Classify the preparation.
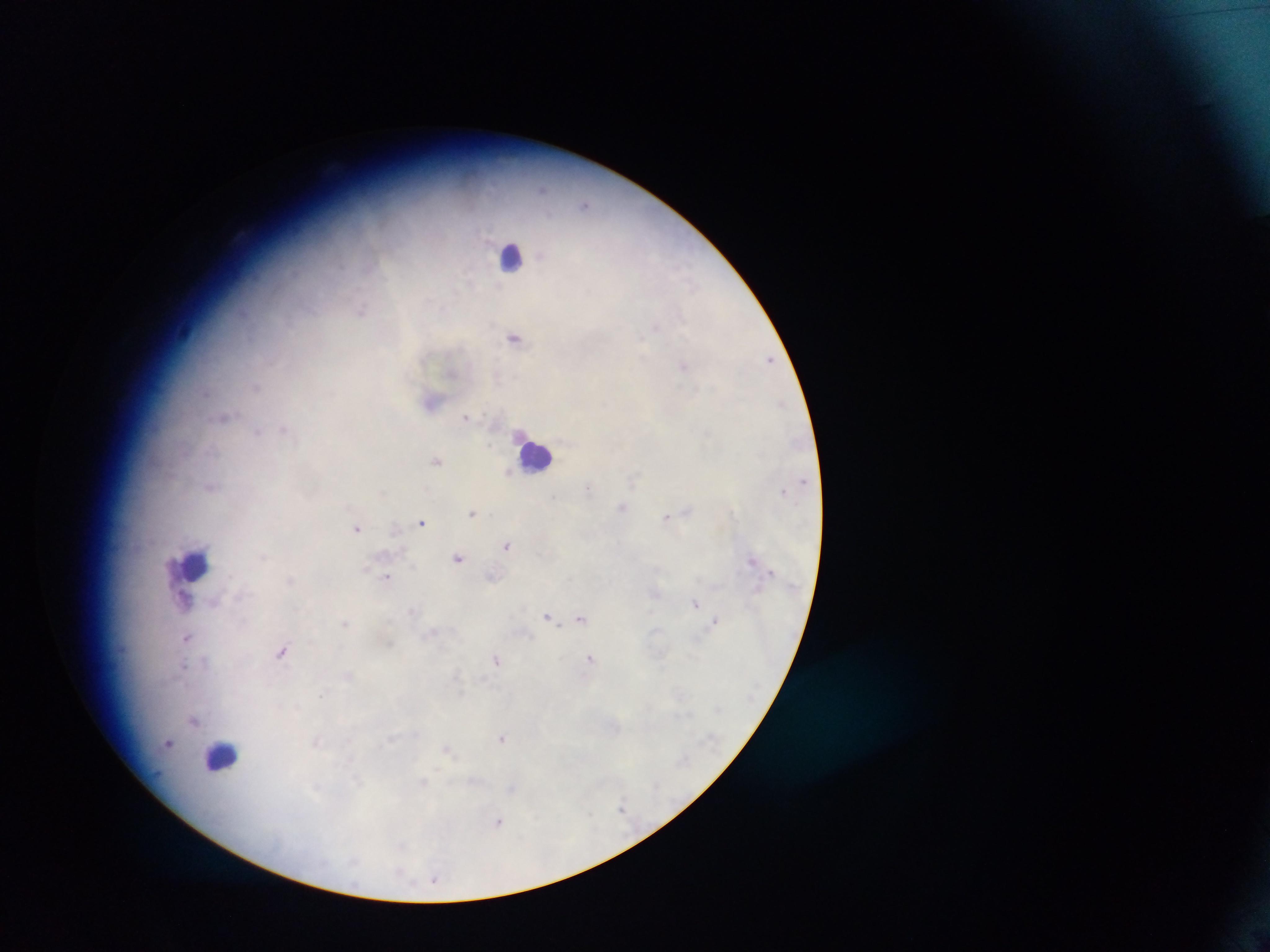
This is a thick smear.

Approximate centers as x y in pixels.
Summary:
  - Plasmodium parasite locations: 545 188; 584 204; 362 307; 680 314; 655 326; 515 337; 772 360; 686 366; 257 385; 695 389; 223 416; 466 417; 283 427; 257 431; 710 436; 438 461; 509 472; 209 485; 590 489; 555 496; 622 507; 688 510; 733 511; 470 513; 666 516; 422 521; 356 528; 506 545; 264 558; 457 559; 752 560; 387 576; 290 579; 187 596; 214 602; 695 602; 547 614; 582 616; 716 620; 345 623; 186 638; 281 650; 592 656; 496 657; 204 661; 185 667; 458 675; 323 692; 194 722; 501 738; 390 739; 169 743; 316 743; 449 748; 358 780; 423 780; 315 788; 621 804; 590 814; 499 822; 401 874; 435 881
  - Leukocyte locations: 508 256; 537 454; 192 564; 222 753
  - Capture: mobile-phone photograph through a microscope
  - Image size: 1270×952 pixels
  - Country: Ghana
  - Field of view: single